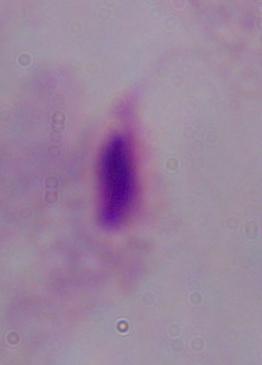
{
  "magnification": "1000x",
  "identification": "trichomonad",
  "modality": "micrograph"
}